Assess the morphology of the erythrocytes.
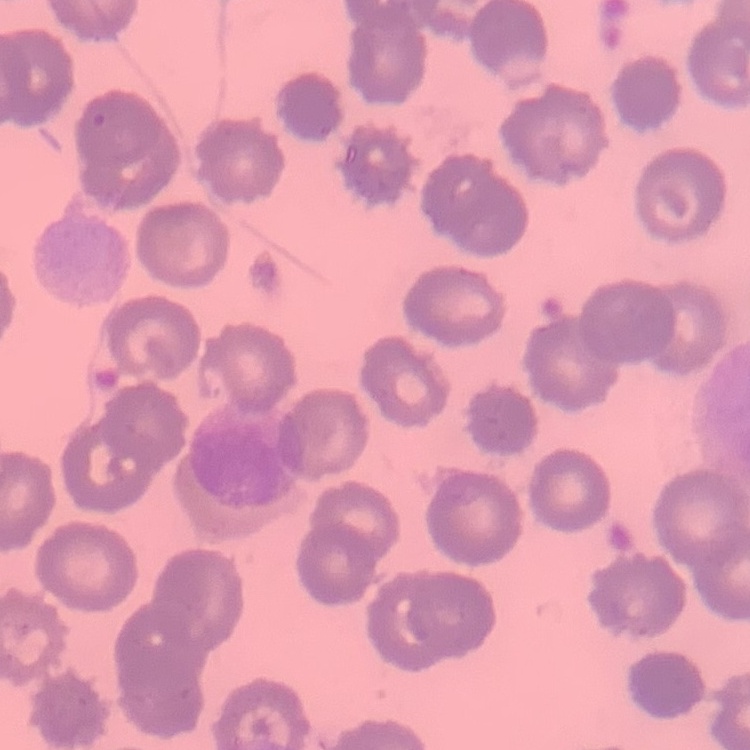

No rouleaux formation.

Square crop of a larger photomicrograph. Stained with either Field's or Giemsa. Thin blood film.